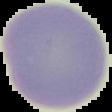
Cell region segmented out of the field of view; the surrounding area is masked to black. Image is 112×112 pixels. From a thin blood film. Malaria status: uninfected.